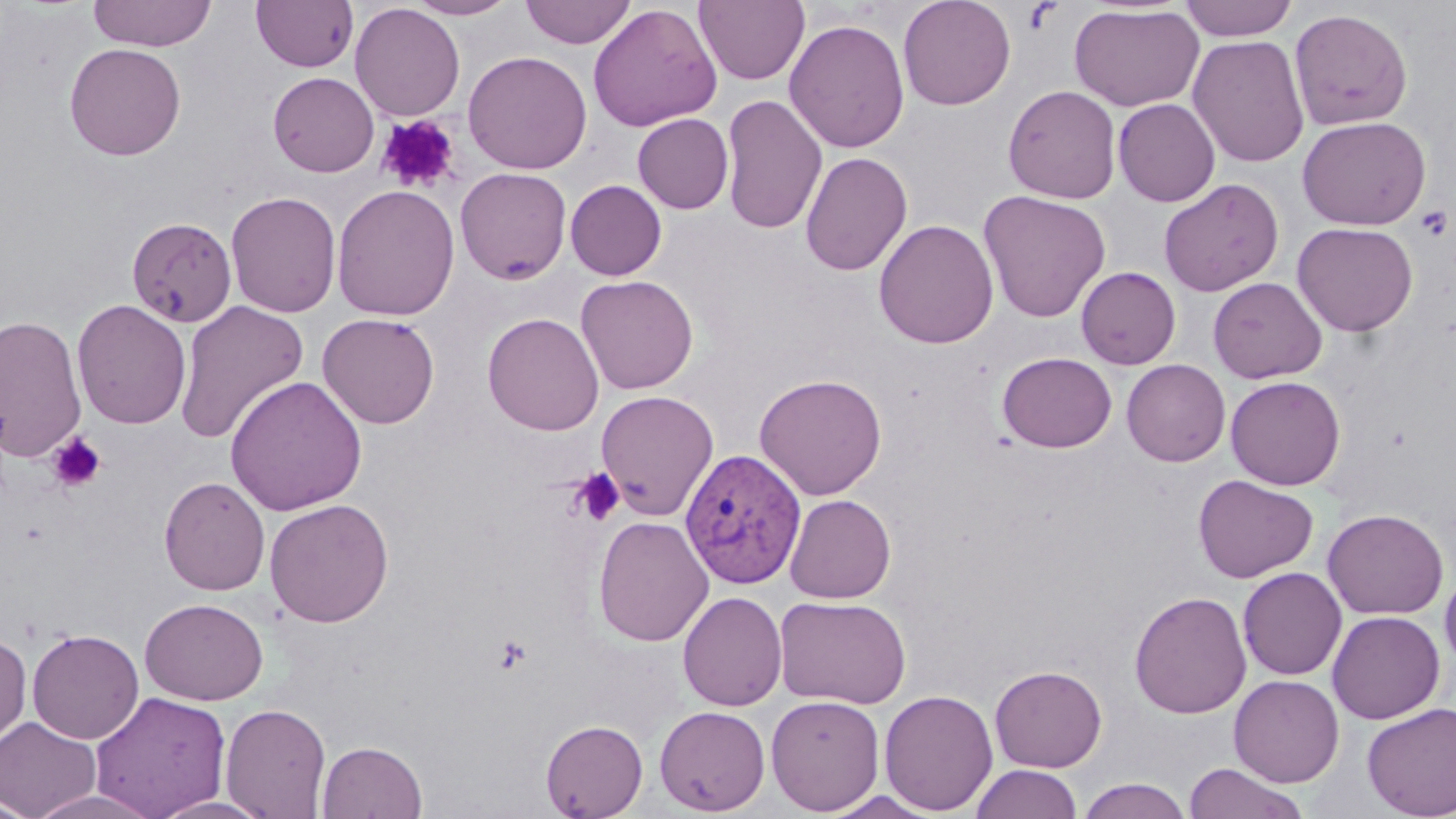
slide-level diagnosis = Plasmodium vivax
image size = 1456×819 pixels
platelet locations = approximate bounding boxes as (x1,y1)-(x2,y2) corner pairs in pixels: (377,114)-(460,193), (1414,205)-(1452,242), (47,433)-(106,493), (568,468)-(626,527), (492,634)-(532,675)
preparation = thin blood smear
magnification = 1000x
field of view = one of a larger specimen
stain = May-Grünwald-Giemsa
modality = optical microscopy
Plasmodium vivax-infected red blood cell locations = approximate bounding boxes as (x1,y1)-(x2,y2) corner pairs in pixels: (680,448)-(807,589)
uninfected red blood cell locations = approximate bounding boxes as (x1,y1)-(x2,y2) corner pairs in pixels: (88,0)-(216,52), (251,0)-(358,72), (405,0)-(520,20), (521,0)-(636,48), (694,0)-(809,86), (898,0)-(1016,110), (1179,0)-(1298,41), (349,3)-(465,121), (587,3)-(722,132), (1069,4)-(1204,112), (1289,8)-(1413,130), (784,18)-(910,153), (1188,34)-(1309,168), (64,42)-(186,160), (462,50)-(592,175), (268,71)-(379,177), (1002,84)-(1122,203), (720,94)-(828,235), (1113,98)-(1220,206), (633,113)-(733,214), (1297,116)-(1431,230), (800,151)-(913,276), (454,167)-(572,284), (1159,178)-(1284,297), (565,180)-(667,280), (331,184)-(460,321), (225,190)-(342,318), (978,190)-(1111,323), (126,216)-(237,328), (873,218)-(999,349), (1292,222)-(1418,336), (1075,266)-(1181,370), (575,275)-(699,395), (1208,277)-(1327,384), (71,299)-(192,429), (173,300)-(309,445), (318,312)-(440,429), (482,312)-(604,436), (0,314)-(87,462), (997,352)-(1117,453), (1121,359)-(1230,466), (754,372)-(888,501), (224,375)-(367,515), (1225,376)-(1346,489), (595,390)-(719,520), (1193,474)-(1318,583), (159,476)-(270,595), (784,494)-(896,604), (264,498)-(394,627), (1322,508)-(1448,619), (593,515)-(713,647), (1440,566)-(1456,673), (1237,567)-(1347,680), (1129,590)-(1251,719), (678,591)-(787,711), (773,595)-(911,709), (139,597)-(268,705), (1326,610)-(1446,724), (27,628)-(145,744), (0,630)-(32,750), (990,665)-(1107,772), (1229,675)-(1344,787), (878,688)-(999,815), (90,691)-(231,818), (765,694)-(885,815), (220,702)-(332,818), (1362,702)-(1456,818), (654,705)-(771,816), (0,717)-(101,819), (540,719)-(648,818), (316,740)-(428,818), (1182,762)-(1309,819), (969,764)-(1083,819), (1077,777)-(1192,818), (27,790)-(164,819), (820,791)-(943,818), (0,793)-(38,819), (146,794)-(280,819)